Assess this cell for malaria.
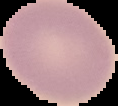

It is uninfected.

image size = 118×106 pixels
preparation = thin blood smear
image type = cell region segmented out of the field of view; surrounding area masked to black